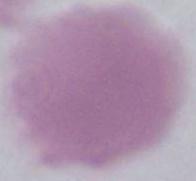

Summary:
  - Modality: photomicrograph
  - Magnification: 1000x
  - Identification: erythrocyte